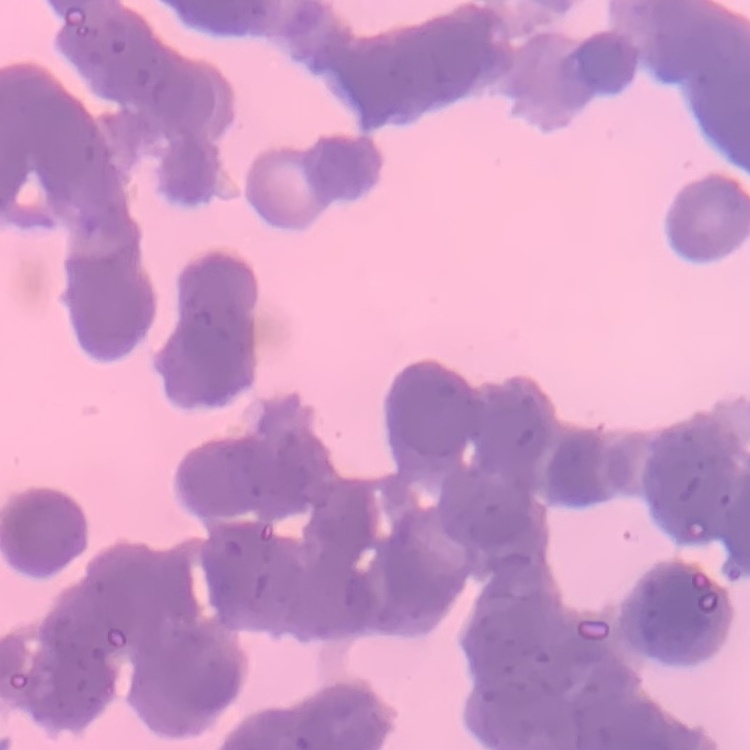
Summary:
  - Red blood cell morphology: rouleaux formation
  - Preparation: thin blood smear
  - Image type: one tile cut from a larger photomicrograph
  - Stain: Field's or Giemsa